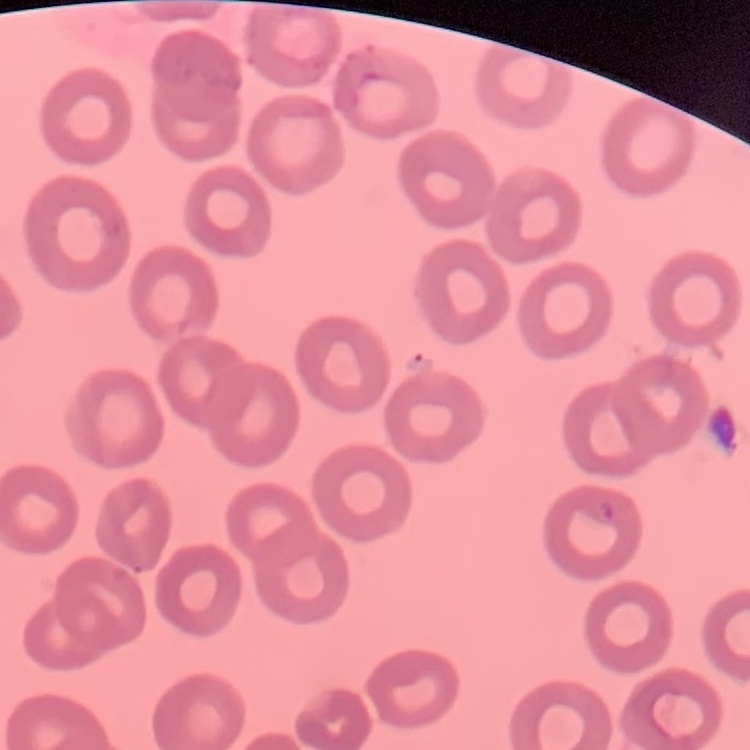
red blood cell morphology = no rouleaux formation
stain = Field's or Giemsa
image type = one tile cut from a larger photomicrograph
preparation = thin peripheral smear